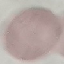
Summary:
  - Malaria status: uninfected
  - Stain: Giemsa
  - Image type: cell patch, automatically extracted from a larger field of view and resized to 64 × 64 pixels
  - Capture: smartphone camera at the microscope eyepiece
  - Preparation: thin smear